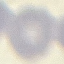

Summary:
  - Result: no malaria parasites seen
  - Preparation: thin blood smear
  - Capture: smartphone through the microscope eyepiece
  - Image type: cell patch, automatically extracted from a larger field of view and resized to 64 × 64 pixels
  - Stain: Giemsa